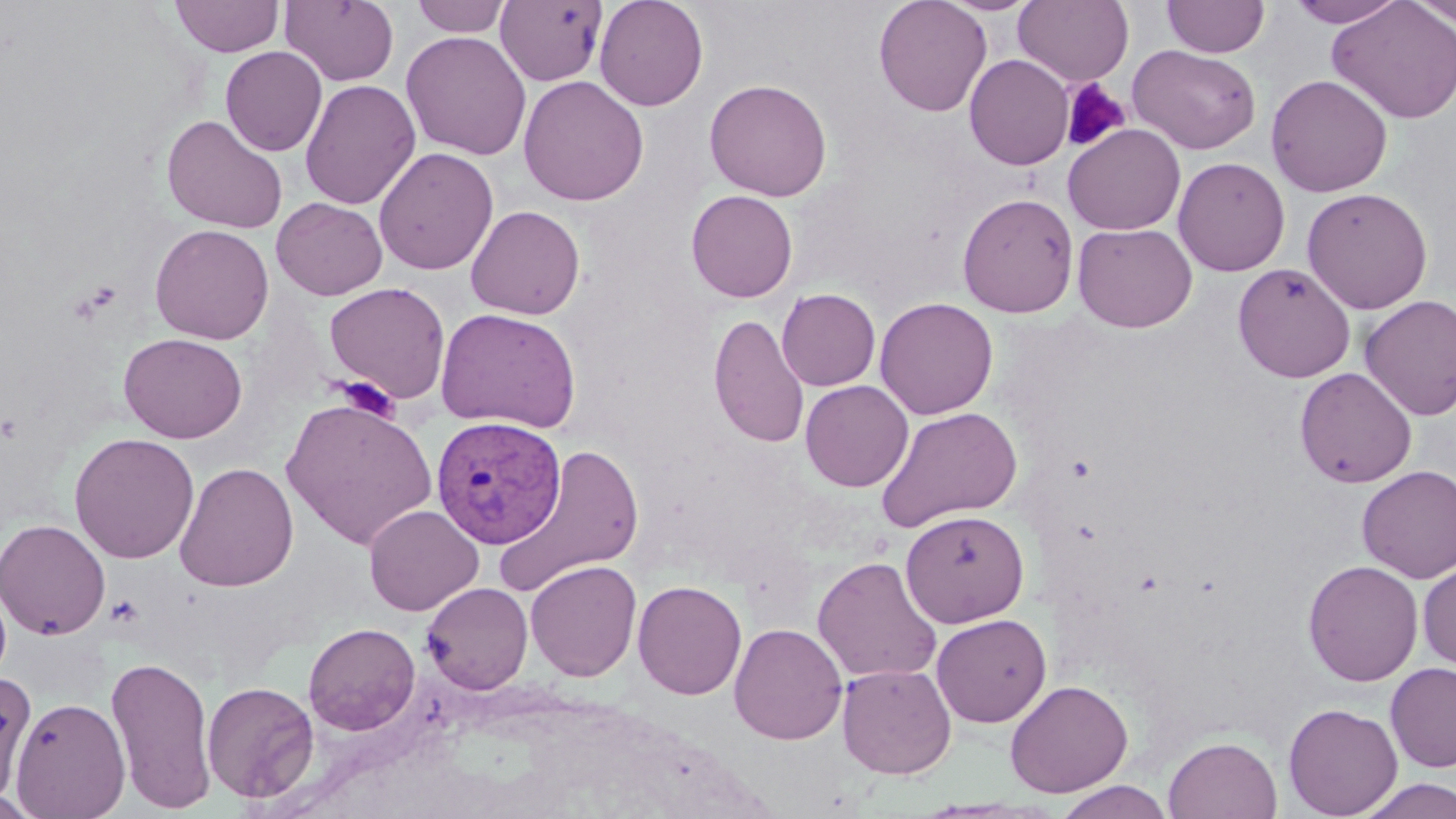

slide_level_diagnosis: Plasmodium vivax
modality: light microscopy
uninfected_red_blood_cell_locations: 'approximate bounding boxes as (x1,y1)-(x2,y2) corner pairs in pixels: (170,0)-(284,57), (411,0)-(512,37), (594,0)-(709,111), (873,0)-(992,117), (938,0)-(1041,16), (1013,0)-(1134,86), (1162,0)-(1270,58), (1286,0)-(1408,28), (1327,0)-(1456,125), (1408,0)-(1456,28), (280,1)-(400,86), (495,1)-(607,86), (401,30)-(532,160), (1128,44)-(1261,154), (220,46)-(327,156), (964,54)-(1074,170), (1265,74)-(1393,197), (518,75)-(649,206), (703,78)-(832,201), (300,79)-(421,210), (161,114)-(288,233), (1063,124)-(1186,235), (373,147)-(498,275), (1173,157)-(1290,276), (1301,187)-(1433,313), (686,190)-(798,302), (957,191)-(1079,317), (271,197)-(388,300), (466,205)-(585,319), (1073,222)-(1197,333), (149,223)-(274,344), (1232,262)-(1356,382), (324,281)-(451,403), (777,288)-(880,391), (1358,295)-(1456,420), (874,297)-(998,419), (435,307)-(580,433), (708,312)-(811,449), (118,332)-(248,443), (1294,367)-(1417,488), (800,380)-(914,492), (281,396)-(437,549), (875,406)-(1023,532), (68,432)-(200,564), (494,443)-(646,598), (174,462)-(299,592), (1356,465)-(1456,583), (363,504)-(483,616), (900,509)-(1029,627), (0,518)-(111,640), (811,556)-(943,685), (525,559)-(642,681), (1302,560)-(1423,686), (1417,561)-(1456,671), (632,579)-(747,700), (422,582)-(533,695), (931,613)-(1052,727), (303,622)-(420,735), (729,622)-(847,745), (106,653)-(218,813), (837,662)-(956,779), (1386,662)-(1456,772), (0,672)-(36,803), (202,680)-(319,803), (1004,680)-(1134,798), (9,696)-(131,818), (1283,703)-(1402,817), (1163,734)-(1283,819), (1356,777)-(1456,818), (1053,780)-(1175,819)'
preparation: thin blood film
image_size: 1456×819 pixels
platelet_locations: 'approximate bounding boxes as (x1,y1)-(x2,y2) corner pairs in pixels: (1061,79)-(1130,153), (78,280)-(123,316), (332,377)-(399,420)'
magnification: 1000x
field_of_view: one of a larger specimen
stain: May-Grünwald-Giemsa
plasmodium_vivax_infected_red_blood_cell_locations: 'approximate bounding boxes as (x1,y1)-(x2,y2) corner pairs in pixels: (430,414)-(567,548)'